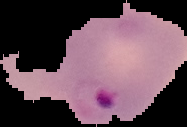
Summary:
  - Image type: segmented cell region on a black background
  - Malaria status: parasitized
  - Preparation: thin blood film
  - Image size: 187×127 pixels